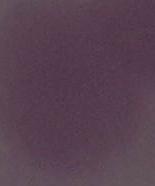
Summary:
  - Modality: photomicrograph
  - Identification: red blood cell
  - Magnification: 1000x